Name the blood parasite species.
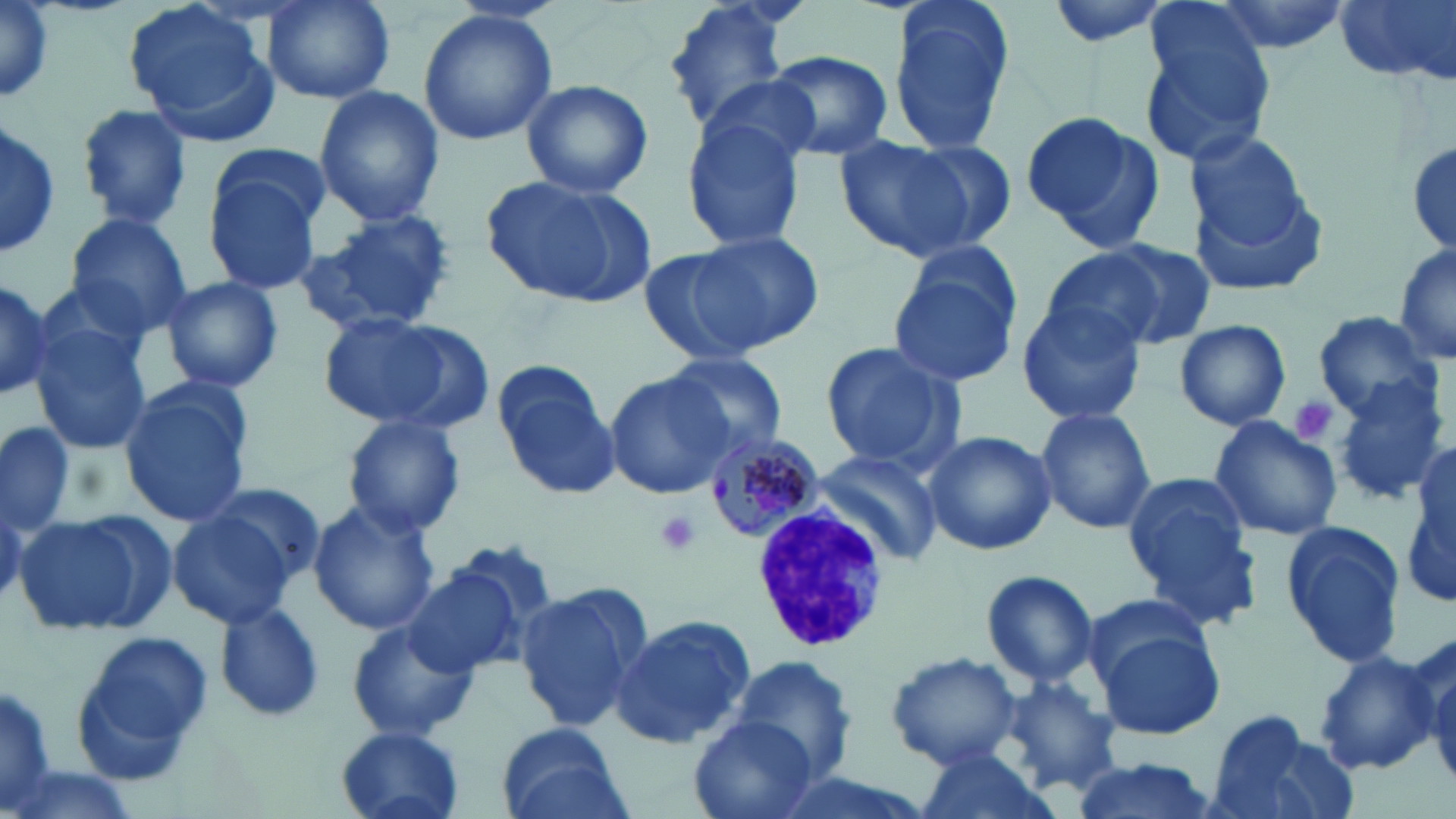

Plasmodium malariae.

Summary:
  - Coordinate format: approximate bounding boxes as (x1, y1, x2, y2) in pixels
  - Uninfected red blood cell locations: (259, 0, 396, 106), (660, 0, 804, 136), (885, 0, 1016, 157), (1045, 0, 1176, 49), (1207, 0, 1354, 56), (1335, 0, 1454, 86), (0, 1, 56, 105), (1134, 2, 1280, 167), (125, 5, 281, 144), (417, 9, 558, 144), (763, 50, 893, 161), (520, 78, 653, 200), (313, 86, 444, 226), (75, 104, 192, 231), (681, 110, 811, 252), (1021, 111, 1165, 249), (0, 118, 59, 259), (1406, 130, 1456, 266), (838, 134, 1005, 261), (1186, 138, 1322, 284), (212, 144, 334, 240), (201, 164, 325, 296), (481, 173, 655, 310), (292, 210, 459, 338), (63, 213, 191, 338), (684, 229, 825, 352), (1098, 238, 1217, 348), (1393, 241, 1456, 370), (888, 242, 1026, 387), (636, 245, 774, 369), (1037, 248, 1168, 354), (161, 276, 284, 393), (0, 279, 55, 396), (1014, 298, 1147, 425), (1313, 311, 1440, 419), (312, 312, 488, 432), (30, 314, 154, 459), (1173, 318, 1291, 431), (819, 342, 964, 470), (660, 352, 789, 455), (490, 358, 621, 500), (1328, 369, 1451, 506), (604, 372, 734, 499), (117, 378, 256, 528), (1033, 405, 1157, 535), (1207, 414, 1342, 544), (341, 415, 468, 539), (0, 419, 78, 535), (921, 430, 1058, 556), (810, 447, 945, 566), (1403, 451, 1456, 615), (1124, 472, 1259, 614), (197, 479, 328, 594), (307, 498, 439, 636), (166, 503, 303, 631), (16, 508, 169, 639), (1280, 519, 1408, 667), (400, 564, 526, 679), (981, 569, 1100, 689), (513, 587, 649, 730), (1081, 589, 1215, 688), (212, 600, 326, 725), (609, 616, 752, 751), (347, 618, 479, 743), (1092, 624, 1226, 741), (1043, 627, 1198, 778), (69, 629, 213, 785), (1413, 630, 1455, 783), (1311, 650, 1437, 775), (885, 651, 1024, 769), (728, 657, 859, 784), (1000, 675, 1124, 795), (0, 676, 61, 819), (1202, 711, 1347, 819), (688, 715, 818, 819), (496, 724, 629, 819), (335, 726, 467, 819), (909, 744, 1057, 819), (1066, 758, 1220, 819)
  - Plasmodium malariae-infected red blood cell locations: (704, 427, 823, 547)
  - Platelet locations: (1290, 396, 1337, 445), (651, 509, 704, 558)
  - White blood cell locations: (750, 503, 888, 654)
  - Stain: May-Grünwald-Giemsa
  - Field of view: one of a larger specimen
  - Preparation: thin blood film
  - Magnification: 1000x
  - Image size: 1456×819 pixels
  - Modality: light microscopy